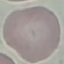

Malaria status: uninfected. Acquired by smartphone through the microscope eyepiece. Cell patch, automatically extracted from a larger field of view and resized to 64 × 64 pixels. Giemsa stain. Thin blood film.